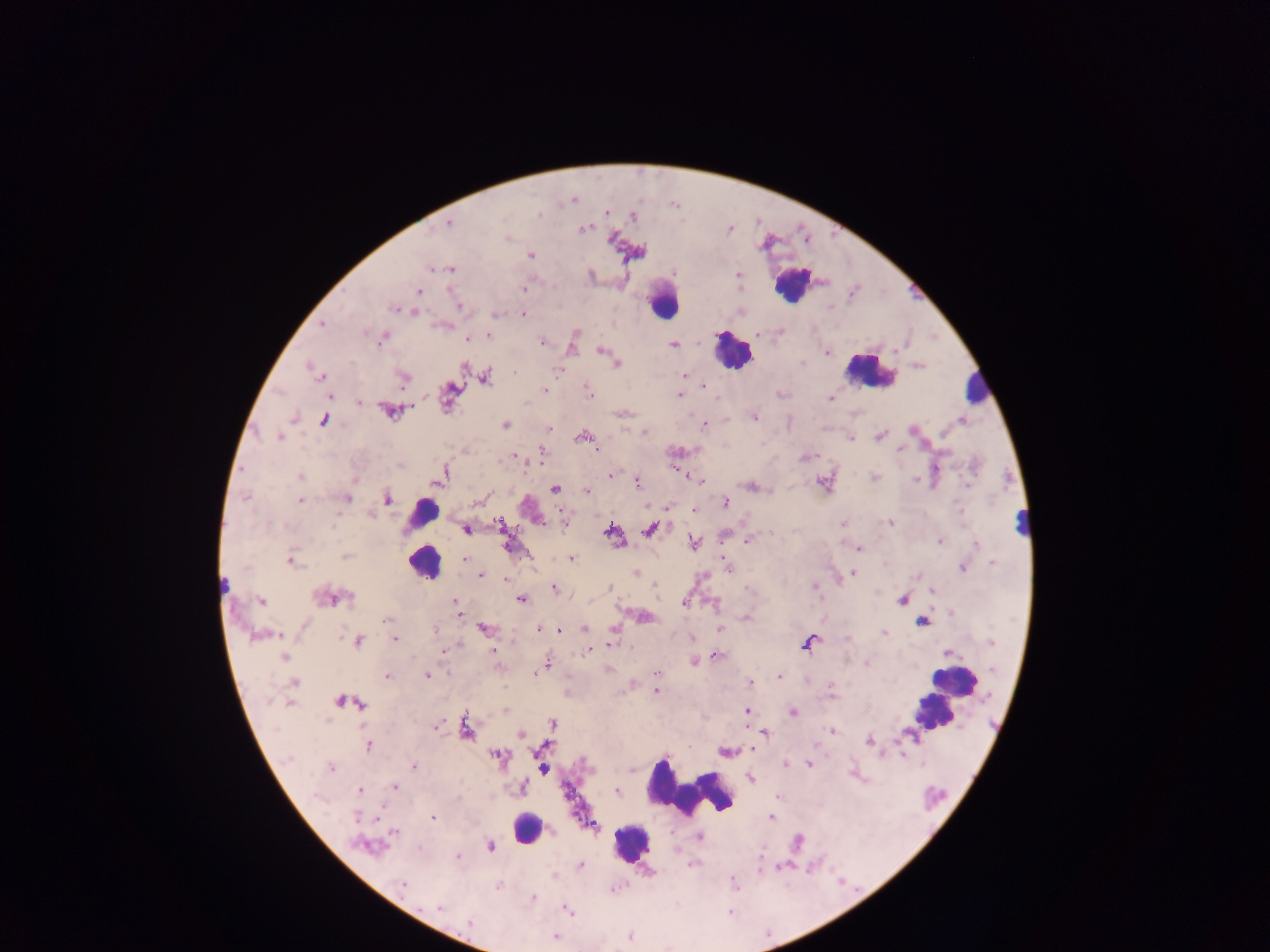

Approximate centers as (x, y) in pixels.
Summary:
  - Malaria parasite locations: (573, 200), (606, 212), (539, 215), (632, 216), (448, 223), (584, 228), (612, 239), (530, 255), (431, 268), (440, 268), (450, 269), (739, 274), (524, 288), (418, 292), (458, 306), (395, 309), (415, 311), (523, 314), (496, 315), (322, 324), (576, 333), (757, 334), (489, 335), (382, 339), (466, 339), (542, 342), (672, 344), (600, 350), (827, 352), (896, 352), (617, 363), (308, 367), (558, 370), (317, 374), (685, 374), (486, 376), (403, 378), (702, 385), (545, 390), (450, 391), (588, 391), (329, 395), (679, 395), (830, 398), (359, 401), (390, 412), (754, 417), (293, 418), (323, 420), (962, 421), (505, 425), (704, 426), (549, 428), (644, 432), (582, 436), (880, 436), (280, 437), (851, 438), (899, 449), (597, 450), (543, 453), (516, 456), (300, 476), (610, 476), (875, 478), (440, 479), (915, 480), (700, 481), (637, 483), (969, 484), (749, 485), (555, 489), (586, 491), (246, 498), (347, 498), (387, 499), (300, 500), (477, 502), (725, 503), (694, 510), (371, 516), (500, 523), (842, 524), (890, 524), (564, 525), (466, 530), (650, 530), (611, 532), (771, 533), (940, 541), (747, 542), (695, 543), (976, 544), (860, 549), (345, 555), (571, 558), (464, 559), (724, 559), (291, 560), (992, 563), (725, 564), (963, 568), (637, 573), (854, 573), (481, 575), (506, 579), (814, 586), (553, 588), (610, 588), (933, 591), (342, 596), (332, 597), (522, 599), (901, 600), (261, 602), (455, 603), (685, 603), (458, 611), (951, 612), (644, 617), (745, 618), (385, 620), (922, 621), (483, 628), (435, 629), (585, 629), (719, 629), (539, 630), (559, 631), (885, 633), (263, 635), (392, 635), (395, 640), (358, 641), (991, 642), (609, 644), (808, 644), (590, 650), (442, 651), (494, 652), (949, 654), (716, 656), (284, 657), (694, 662), (867, 664), (545, 665), (993, 669), (538, 672), (657, 674), (427, 675), (388, 676), (780, 676), (294, 682), (750, 682), (831, 686), (831, 690), (656, 691), (339, 701), (289, 703), (361, 704), (747, 711), (793, 712), (553, 723), (436, 726), (466, 728), (831, 731), (520, 734), (765, 734), (869, 742), (369, 745), (498, 755), (902, 755), (785, 763), (809, 764), (414, 767), (331, 768), (543, 769), (751, 779), (394, 786), (523, 788), (359, 791), (616, 792), (357, 817), (433, 817), (771, 817), (593, 826), (393, 833), (700, 837), (365, 845), (490, 846), (419, 849), (458, 857), (580, 865), (733, 880), (403, 883), (498, 886), (532, 898), (439, 908), (568, 911), (469, 922), (555, 937), (630, 937)
  - Leukocyte locations: (795, 277), (663, 302), (732, 351), (869, 373), (979, 387), (423, 511), (1022, 520), (424, 564), (226, 586), (952, 681), (931, 712), (691, 791), (527, 826), (632, 843)
  - Preparation: thick blood film
  - Field of view: single
  - Image size: 1270×952 pixels
  - Country: Ghana
  - Capture: mobile-phone photograph through a microscope